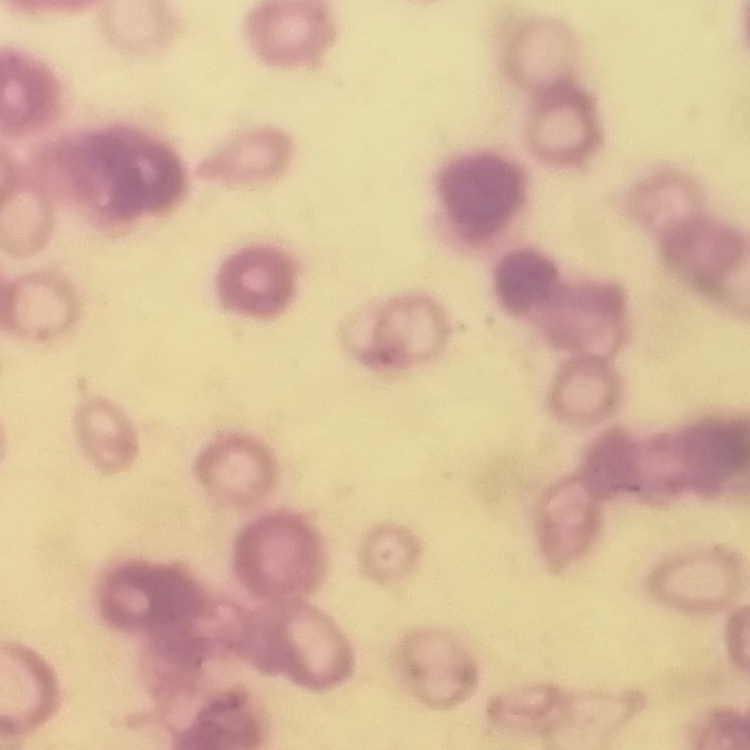
The erythrocytes show rouleaux formation. Stained with either Field's or Giemsa. Square crop of a larger photomicrograph. Thin peripheral smear.